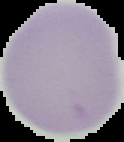

malaria_status: uninfected
image_size: 124×142 pixels
image_type: segmented cell region on a black background
preparation: thin blood film